Assess this cell for malaria.
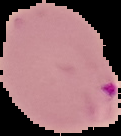

It is parasitized.

Summary:
  - Image type: cell region segmented out of the field of view; surrounding area masked to black
  - Image size: 121×136 pixels
  - Preparation: thin blood smear